Comment on the morphology of the red blood cells.
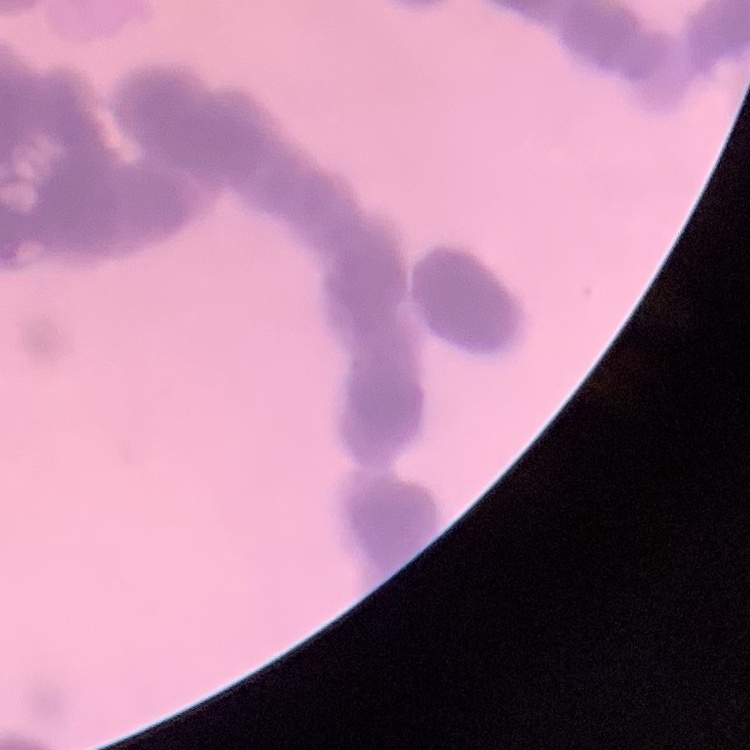

They show rouleaux formation.

Summary:
  - Stain: Field's or Giemsa
  - Preparation: thin peripheral smear
  - Image type: one tile cut from a larger photomicrograph